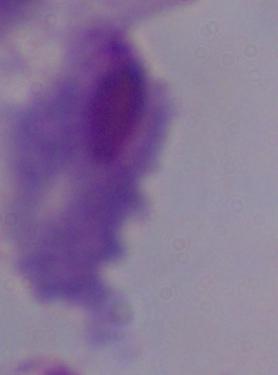
magnification = 1000x
identification = trichomonad
modality = photomicrograph